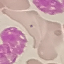

Malaria status: uninfected. Cell patch, automatically extracted from a larger field of view and resized to 64 × 64 pixels. Giemsa-stained preparation. Photographed with a smartphone camera at the microscope eyepiece. Thin blood smear.